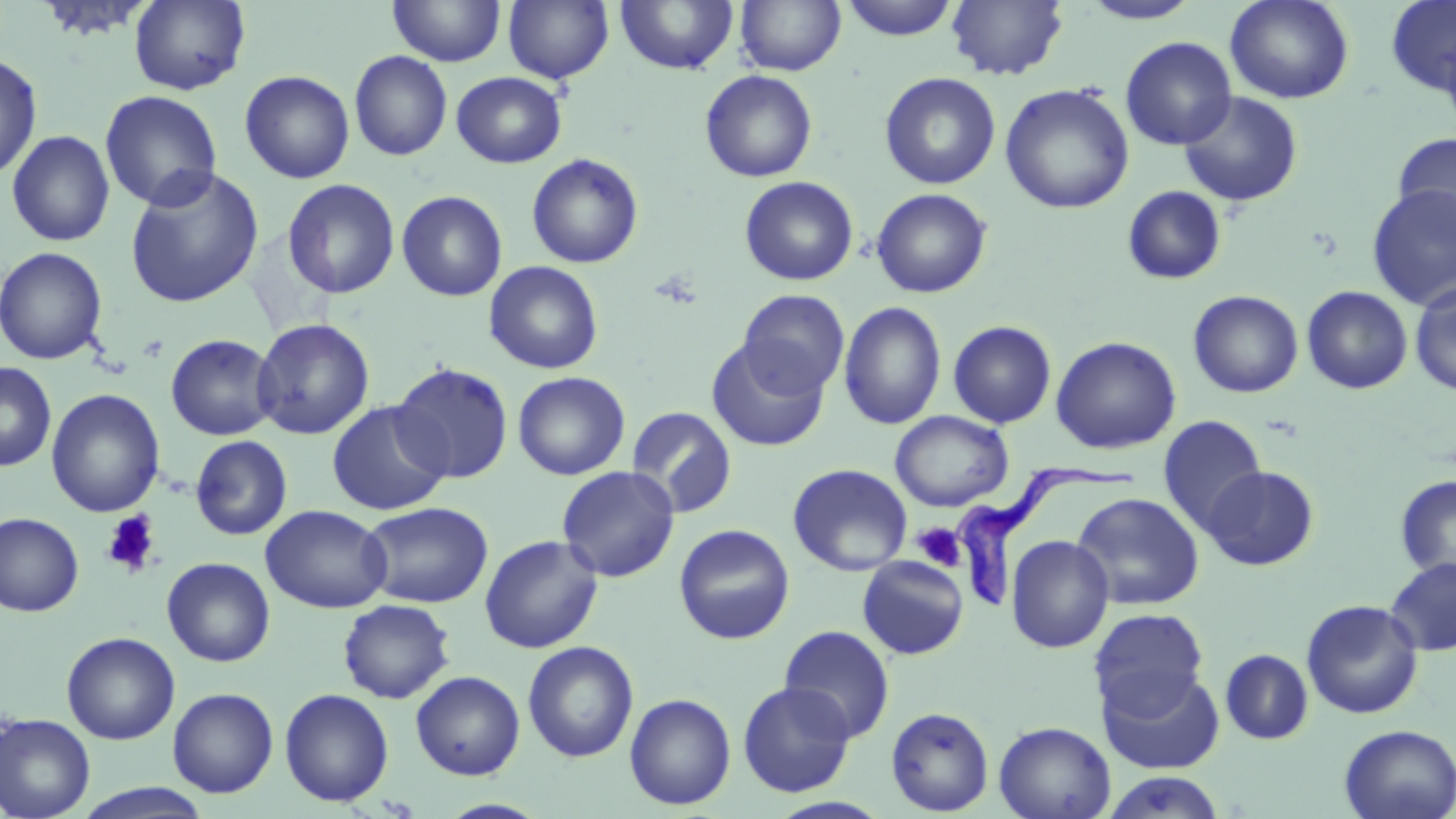
Summary:
  - Coordinate format: approximate bounding boxes as (x1, y1, x2, y2) in pixels
  - Uninfected red blood cell locations: (129, 0, 251, 95), (388, 0, 506, 67), (503, 0, 615, 84), (616, 0, 739, 75), (735, 0, 846, 76), (841, 0, 959, 41), (946, 0, 1069, 80), (1225, 0, 1354, 104), (1079, 1, 1202, 24), (1385, 1, 1456, 99), (1120, 36, 1237, 150), (349, 51, 452, 161), (0, 52, 41, 180), (240, 70, 355, 184), (700, 70, 817, 182), (451, 71, 567, 168), (880, 72, 1000, 190), (1000, 83, 1134, 214), (100, 90, 222, 211), (1178, 91, 1304, 207), (6, 130, 115, 247), (1392, 131, 1456, 238), (526, 153, 644, 269), (124, 166, 265, 309), (739, 176, 859, 286), (281, 178, 400, 299), (1366, 183, 1456, 310), (1122, 186, 1226, 286), (871, 188, 992, 298), (396, 190, 507, 302), (0, 246, 108, 365), (484, 261, 604, 374), (1410, 281, 1456, 397), (1301, 286, 1413, 395), (738, 289, 850, 397), (1188, 290, 1303, 398), (839, 301, 946, 430), (251, 318, 375, 440), (948, 320, 1057, 428), (165, 333, 280, 441), (1050, 336, 1181, 454), (706, 338, 831, 452), (0, 362, 57, 472), (390, 362, 514, 484), (513, 371, 630, 480), (46, 388, 165, 517), (326, 400, 451, 516), (625, 406, 738, 518), (890, 410, 1014, 511), (1158, 416, 1267, 535), (190, 434, 293, 540), (787, 463, 913, 576), (1202, 464, 1319, 571), (556, 466, 680, 582), (1395, 474, 1456, 585), (1072, 492, 1204, 611), (359, 501, 493, 608), (260, 505, 393, 613), (0, 512, 84, 618), (674, 524, 795, 644), (479, 534, 604, 653), (1006, 535, 1114, 653), (857, 556, 970, 660), (161, 557, 275, 667), (1384, 557, 1456, 656), (337, 599, 455, 704), (1301, 599, 1423, 719), (1088, 608, 1209, 717), (778, 625, 896, 743), (62, 631, 180, 744), (523, 640, 639, 763), (1220, 649, 1314, 745), (1098, 667, 1226, 775), (410, 670, 525, 780), (737, 680, 856, 797), (167, 687, 279, 797), (279, 688, 394, 807), (624, 693, 736, 810), (886, 706, 994, 816), (0, 713, 95, 819), (994, 721, 1115, 819), (1338, 724, 1456, 819), (1101, 771, 1227, 819), (72, 783, 216, 818), (437, 799, 552, 818)
  - Trypanosoma brucei locations: (951, 464, 1144, 613)
  - Platelet locations: (100, 511, 160, 576), (913, 523, 965, 570)
  - Slide-level diagnosis: Trypanosoma brucei
  - Preparation: thin blood film
  - Image size: 1456×819 pixels
  - Field of view: single
  - Magnification: 1000x
  - Stain: May-Grünwald-Giemsa
  - Modality: optical microscopy